Assess for malaria.
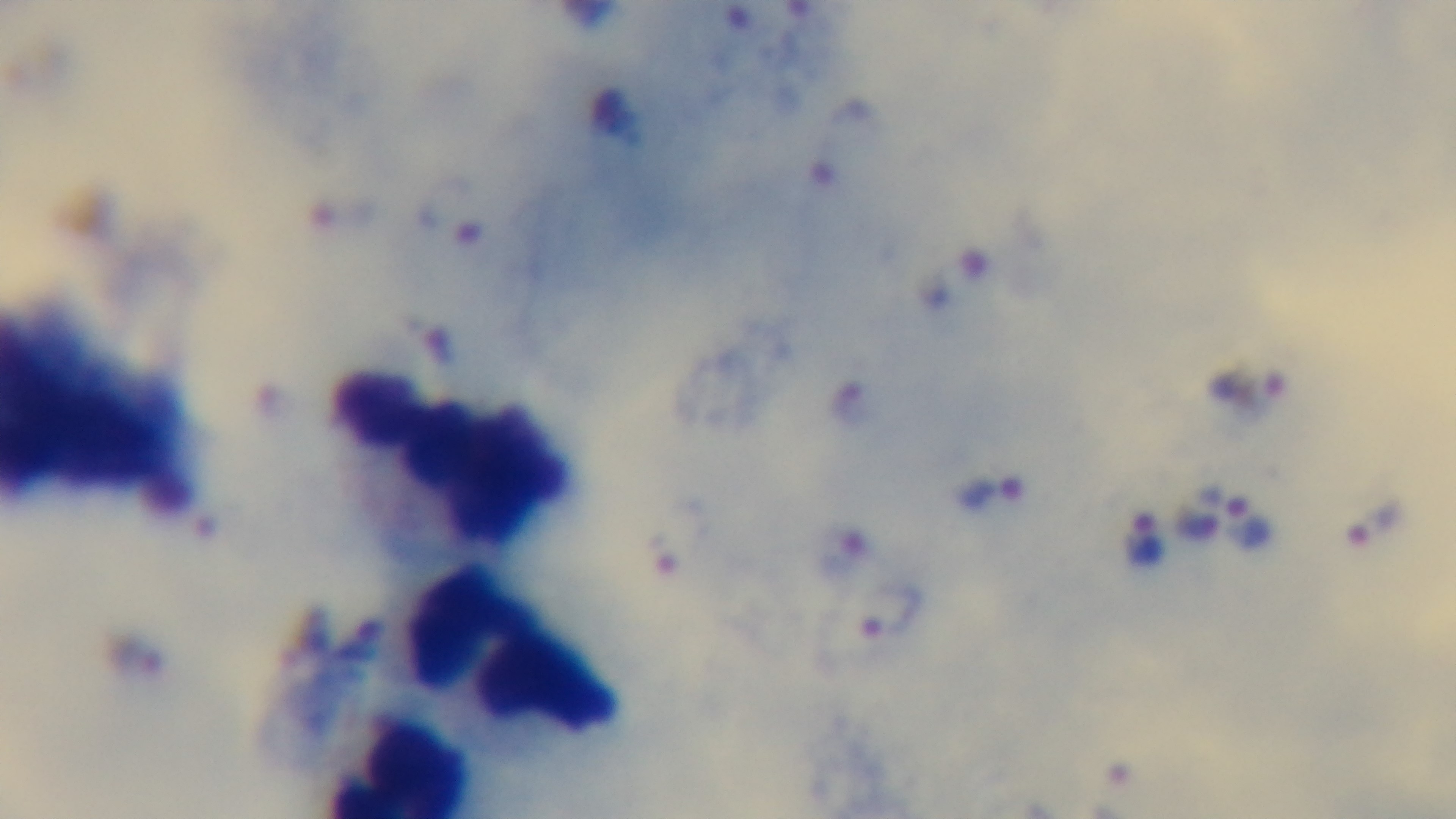

It is infected.

Preparation: thick smear. Oil-immersion objective, 100x. Giemsa stain. Mounted 4K digital camera. Light microscopy. One field from the slide.